Assess this cell for malaria.
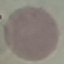

Uninfected.

Thin blood smear. Automatically extracted cell patch, resized to 64 × 64 pixels. Giemsa-stained preparation. Photographed with a smartphone camera at the microscope eyepiece.